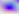
Summary:
  - Identification: Toxoplasma gondii
  - Magnification: 400x
  - Modality: photomicrograph